Name the parasite shown.
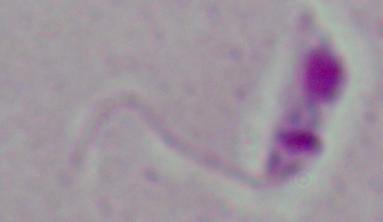

This is Leishmania.

magnification: 1000x
modality: photomicrograph